Outline each Plasmodium malariae-infected red blood cell.
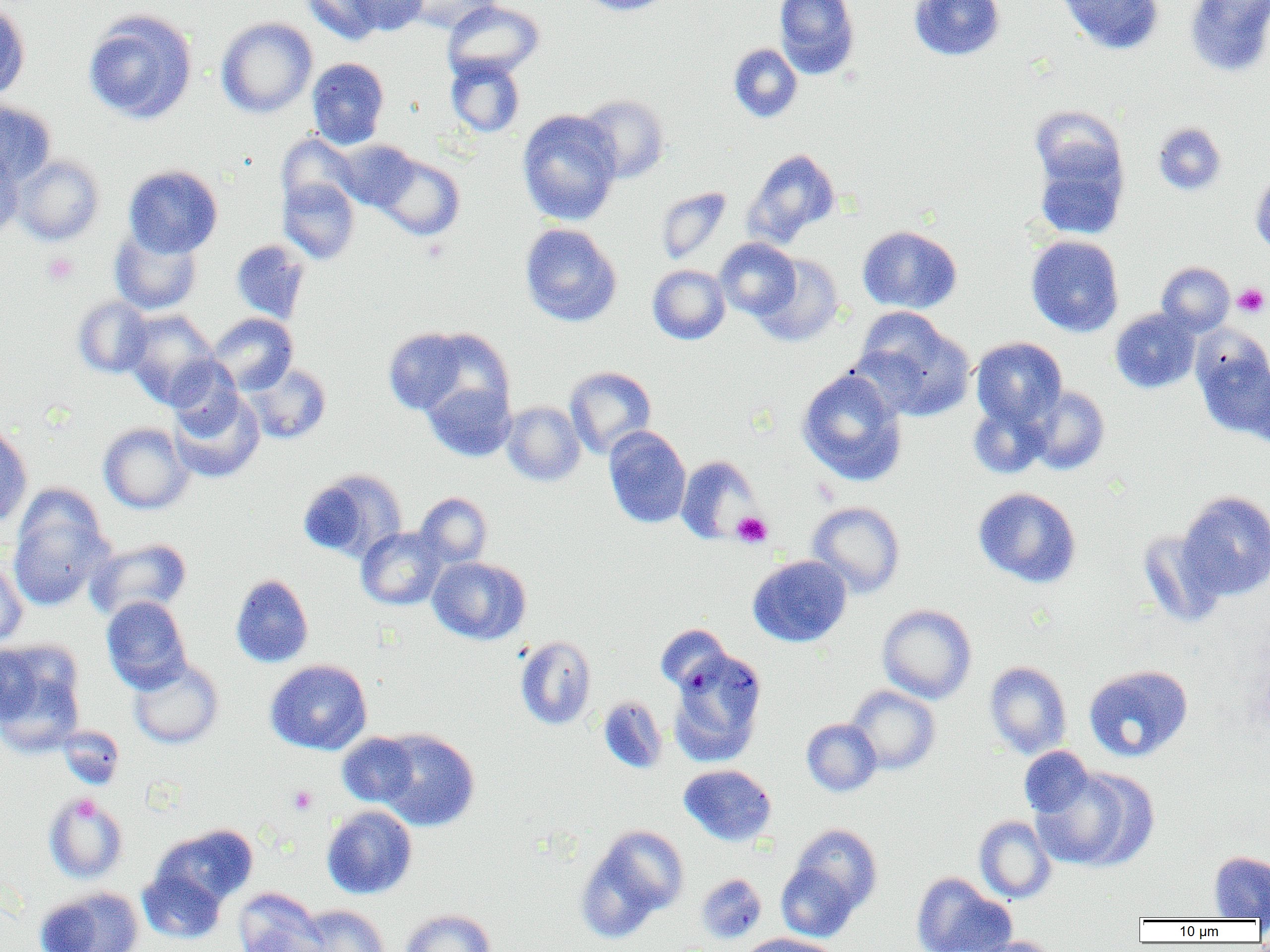

Approximate bounding boxes as [x1, y1, x2, y2] in pixels.
Plasmodium malariae-infected red blood cells: [667, 649, 767, 766].

Uninfected red blood cell locations: [302, 0, 386, 45], [346, 0, 429, 36], [403, 0, 502, 34], [442, 0, 544, 80], [578, 0, 674, 16], [774, 0, 860, 79], [909, 0, 1005, 61], [1057, 0, 1164, 55], [1185, 0, 1270, 77], [0, 2, 30, 102], [83, 10, 197, 125], [216, 17, 317, 118], [728, 43, 803, 123], [445, 55, 525, 137], [306, 57, 389, 149], [577, 94, 669, 183], [0, 100, 56, 185], [1029, 105, 1125, 191], [517, 109, 622, 226], [1153, 121, 1227, 196], [276, 134, 360, 213], [336, 140, 420, 211], [743, 148, 840, 247], [0, 150, 24, 238], [1034, 150, 1127, 240], [13, 154, 105, 245], [373, 154, 465, 241], [123, 165, 223, 257], [1250, 170, 1270, 256], [278, 178, 360, 264], [655, 187, 732, 264], [519, 223, 622, 327], [857, 225, 962, 314], [109, 227, 202, 315], [1026, 235, 1124, 337], [715, 238, 800, 319], [230, 239, 311, 324], [752, 254, 844, 346], [1156, 262, 1234, 336], [647, 264, 730, 344], [73, 296, 153, 378], [851, 308, 974, 422], [122, 309, 220, 408], [1110, 309, 1199, 393], [207, 313, 298, 395], [382, 326, 486, 418], [1192, 331, 1270, 438], [971, 337, 1066, 427], [165, 357, 245, 434], [244, 363, 331, 444], [1244, 363, 1270, 448], [564, 366, 656, 458], [797, 369, 907, 486], [421, 380, 516, 461], [1026, 386, 1110, 474], [168, 388, 265, 483], [968, 401, 1052, 480], [502, 402, 585, 486], [98, 422, 194, 514], [0, 426, 32, 528], [603, 426, 691, 529], [676, 456, 761, 544], [298, 468, 407, 563], [973, 487, 1081, 588], [1178, 490, 1270, 600], [8, 491, 113, 611], [415, 492, 492, 568], [807, 501, 905, 598], [356, 527, 447, 610], [1138, 529, 1227, 627], [87, 538, 191, 620], [748, 555, 852, 647], [0, 557, 28, 647], [427, 557, 531, 645], [230, 573, 313, 667], [101, 596, 191, 692], [878, 604, 977, 704], [654, 624, 731, 694], [515, 636, 597, 730], [0, 642, 85, 755], [128, 656, 224, 749], [265, 659, 372, 755], [984, 661, 1072, 759], [1083, 664, 1193, 762], [847, 685, 940, 775], [597, 696, 667, 774], [801, 718, 882, 796], [58, 725, 124, 789], [375, 728, 480, 831], [336, 732, 420, 808], [1019, 746, 1095, 819], [678, 764, 776, 846], [1031, 766, 1157, 872], [44, 793, 128, 883], [321, 805, 417, 899], [974, 815, 1057, 903], [790, 824, 883, 914], [153, 825, 258, 908], [577, 825, 688, 941], [1209, 851, 1270, 920], [776, 862, 860, 942], [138, 868, 227, 944], [911, 872, 1015, 952], [696, 873, 766, 943], [34, 886, 145, 952], [233, 888, 325, 952], [296, 904, 390, 952], [400, 908, 496, 952], [737, 933, 840, 952], [966, 936, 1061, 952]. Platelet locations: [41, 251, 79, 286], [1233, 283, 1269, 317], [731, 511, 772, 548], [288, 786, 317, 815], [71, 794, 99, 823]. Slide-level diagnosis: Plasmodium malariae. Single field of view. Thin blood film. Light microscopy. 1000x magnification. Image is 1270×952 pixels.